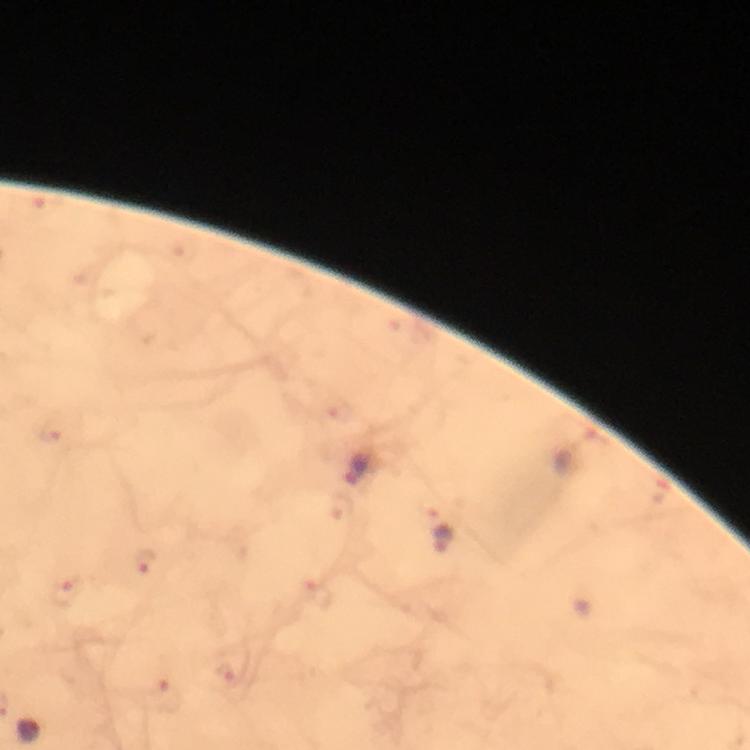

Approximate centers as [x, y] in pixels. Plasmodium parasite locations: [43, 208], [52, 432], [359, 467], [662, 494], [444, 539], [147, 562], [65, 591], [171, 697]. At 100x magnification. Thick blood film. Cropped region of a single field of view. Photographed through the microscope with a smartphone camera. From a malaria diagnostic workup. Image is 750×750 pixels. Giemsa stain. Immersion oil applied.